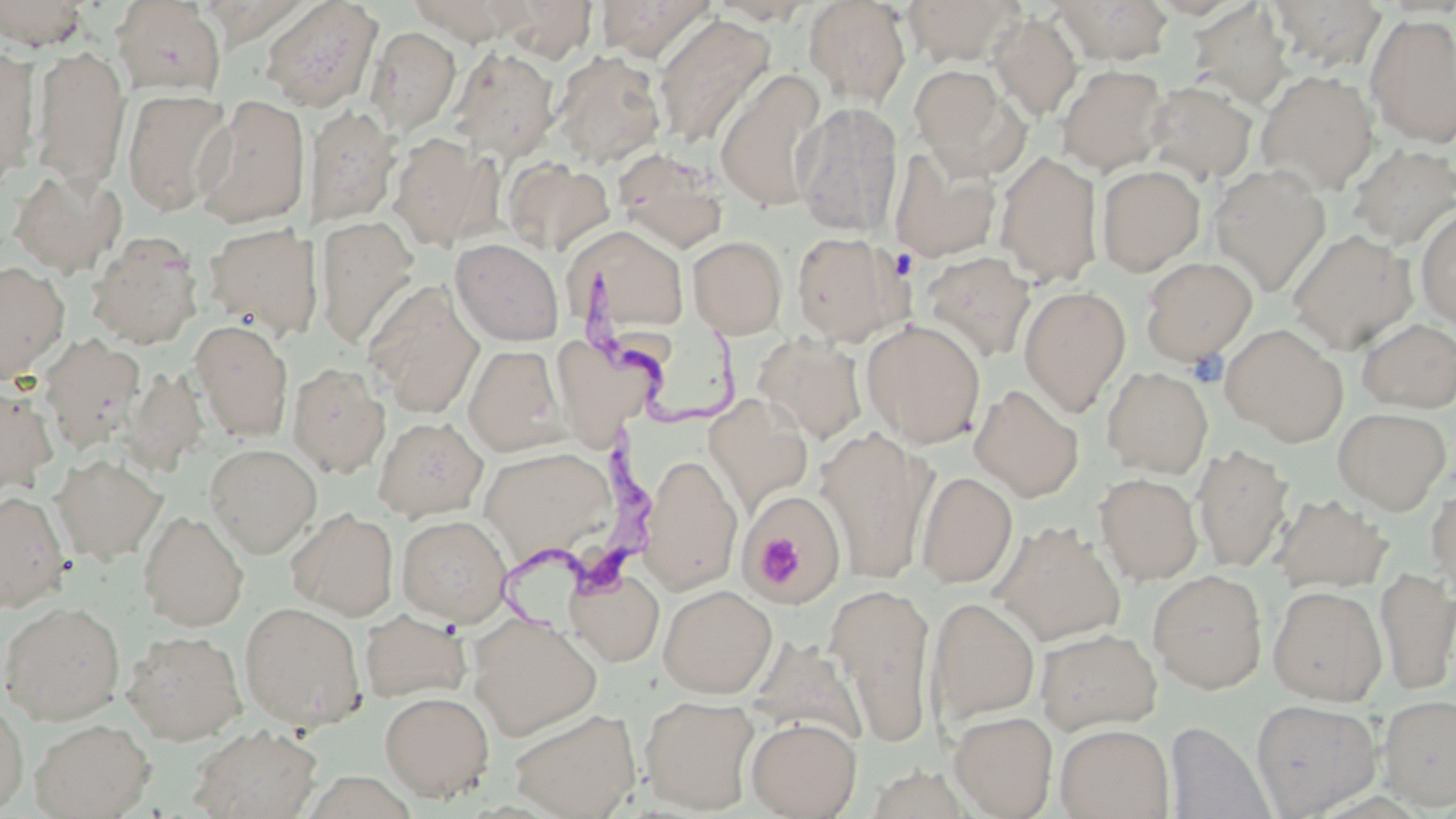

Summary:
  - Coordinate format: approximate bounding boxes as (x1, y1, x2, y2) in pixels
  - Uninfected red blood cell locations: (261, 0, 383, 112), (407, 0, 530, 44), (497, 0, 598, 61), (595, 0, 715, 62), (708, 0, 815, 25), (804, 0, 911, 106), (903, 0, 1022, 66), (1267, 0, 1387, 72), (0, 1, 90, 49), (111, 1, 226, 98), (1056, 1, 1175, 65), (1185, 2, 1294, 110), (990, 13, 1082, 120), (653, 14, 775, 150), (1366, 15, 1456, 148), (367, 27, 461, 134), (0, 46, 40, 188), (31, 46, 130, 191), (449, 47, 560, 160), (553, 51, 666, 168), (1057, 64, 1169, 175), (909, 65, 1017, 173), (714, 69, 826, 212), (1256, 70, 1378, 194), (1145, 80, 1258, 185), (122, 88, 233, 217), (194, 95, 311, 229), (792, 102, 904, 236), (305, 104, 401, 228), (388, 133, 495, 250), (1348, 144, 1456, 250), (889, 146, 1001, 263), (613, 151, 728, 253), (994, 151, 1104, 286), (501, 157, 613, 256), (1209, 164, 1331, 296), (1096, 165, 1205, 276), (8, 168, 127, 276), (1415, 206, 1456, 329), (315, 215, 421, 350), (202, 222, 322, 341), (565, 225, 690, 343), (1287, 230, 1417, 354), (791, 231, 910, 345), (86, 232, 203, 349), (688, 235, 787, 338), (450, 238, 564, 346), (921, 252, 1036, 362), (1141, 256, 1257, 365), (0, 261, 69, 383), (364, 282, 484, 417), (1018, 285, 1131, 416), (190, 318, 294, 441), (1356, 318, 1456, 413), (861, 319, 986, 448), (1222, 324, 1348, 446), (549, 333, 666, 439), (753, 333, 869, 443), (39, 334, 146, 454), (464, 344, 568, 455), (288, 362, 390, 478), (122, 366, 208, 476), (1102, 366, 1213, 478), (0, 383, 59, 498), (969, 384, 1084, 502), (705, 396, 815, 513), (1332, 407, 1451, 513), (373, 416, 487, 522), (815, 428, 936, 585), (205, 443, 321, 557), (1192, 443, 1294, 572), (478, 445, 619, 569), (640, 453, 742, 594), (52, 454, 166, 564), (915, 470, 1018, 588), (1095, 472, 1203, 584), (1426, 482, 1456, 599), (0, 490, 69, 612), (1271, 494, 1392, 595), (742, 495, 843, 608), (286, 507, 399, 620), (138, 510, 248, 630), (396, 513, 512, 625), (991, 520, 1127, 647), (565, 567, 664, 666), (1375, 567, 1456, 695), (1148, 569, 1268, 693), (825, 583, 937, 747), (658, 584, 777, 698), (1268, 585, 1387, 705), (926, 596, 1039, 729), (0, 601, 125, 725), (240, 601, 366, 730), (359, 609, 470, 702), (468, 614, 602, 739), (1035, 627, 1163, 735), (122, 630, 247, 745), (379, 690, 494, 800), (640, 694, 759, 814), (1378, 695, 1456, 812), (0, 696, 28, 815), (1250, 699, 1382, 816), (509, 707, 641, 819), (949, 711, 1057, 817), (746, 717, 862, 819), (29, 718, 154, 818), (1164, 722, 1276, 819), (189, 724, 321, 818), (1055, 724, 1175, 819)
  - Trypanosoma brucei locations: (575, 267, 756, 426), (473, 426, 658, 637)
  - Platelet locations: (1186, 349, 1228, 388), (752, 528, 807, 589)
  - Slide-level diagnosis: Trypanosoma brucei
  - Field of view: single
  - Stain: May-Grünwald-Giemsa
  - Modality: light microscopy
  - Magnification: 1000x
  - Image size: 1456×819 pixels
  - Preparation: thin blood smear